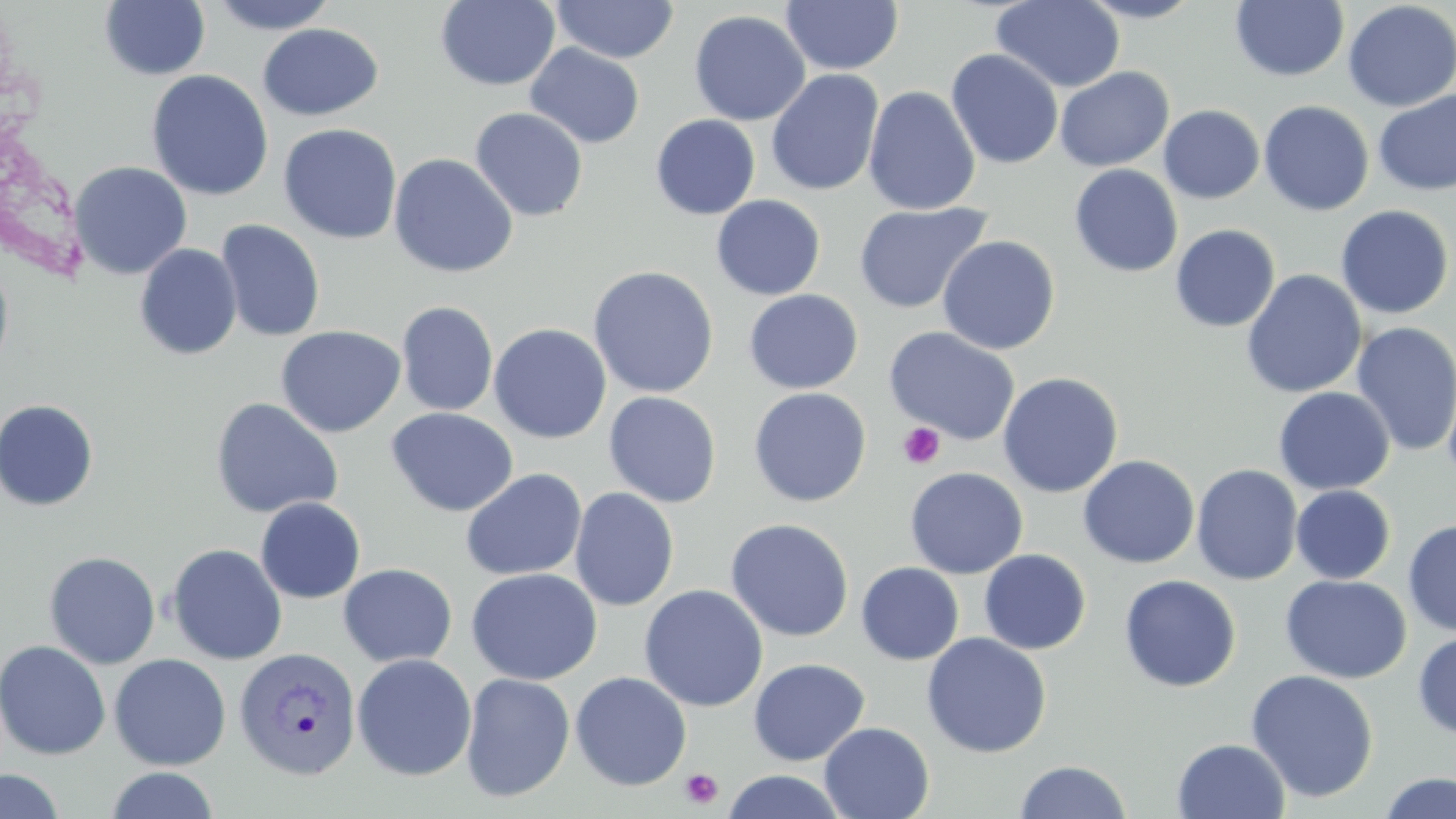 Approximate bounding boxes as [x1, y1, x2, y2] in pixels. Platelet locations: [897, 422, 945, 469], [679, 767, 723, 808]. Uninfected red blood cell locations: [207, 0, 340, 34], [436, 0, 560, 91], [780, 0, 904, 76], [990, 0, 1125, 93], [1077, 0, 1206, 23], [99, 1, 210, 81], [550, 1, 680, 63], [1231, 1, 1349, 82], [1342, 1, 1456, 112], [688, 10, 810, 126], [257, 23, 384, 121], [525, 43, 645, 149], [946, 49, 1064, 169], [1055, 66, 1174, 172], [765, 69, 884, 197], [147, 70, 273, 202], [863, 85, 981, 216], [1373, 89, 1456, 196], [1258, 100, 1374, 216], [1158, 105, 1265, 204], [469, 107, 589, 222], [650, 114, 761, 220], [278, 123, 403, 244], [388, 153, 519, 278], [69, 161, 192, 279], [1069, 164, 1183, 277], [711, 195, 826, 300], [854, 202, 992, 315], [1335, 205, 1455, 320], [216, 219, 326, 342], [1170, 224, 1280, 333], [937, 235, 1060, 355], [134, 243, 242, 361], [0, 260, 14, 379], [587, 265, 720, 398], [1241, 269, 1367, 399], [743, 289, 864, 395], [396, 301, 498, 416], [1351, 321, 1456, 457], [489, 323, 612, 444], [275, 325, 406, 438], [884, 326, 1021, 446], [1439, 354, 1456, 493], [997, 371, 1124, 498], [1273, 386, 1394, 495], [748, 387, 872, 507], [602, 391, 722, 508], [209, 397, 344, 519], [0, 398, 99, 511], [386, 407, 519, 517], [1078, 454, 1200, 569], [1191, 463, 1303, 585], [904, 467, 1028, 579], [460, 468, 587, 581], [1290, 485, 1395, 584], [569, 487, 679, 612], [254, 497, 366, 604], [725, 517, 854, 642], [1403, 518, 1456, 636], [166, 543, 288, 665], [978, 549, 1091, 655], [43, 551, 160, 669], [856, 562, 964, 665], [338, 563, 457, 667], [466, 568, 602, 685], [1119, 574, 1241, 692], [1280, 574, 1412, 684], [639, 584, 768, 712], [1412, 630, 1456, 740], [921, 632, 1051, 758], [0, 640, 111, 760], [108, 653, 231, 771], [352, 653, 476, 781], [747, 658, 870, 766], [1245, 669, 1379, 802], [570, 671, 692, 791], [460, 672, 575, 803], [819, 721, 934, 819], [1172, 738, 1290, 819], [1014, 760, 1133, 819], [104, 767, 221, 818], [0, 769, 66, 818], [721, 770, 848, 818], [1377, 772, 1456, 818]. Plasmodium vivax-infected red blood cell locations: [234, 646, 362, 780]. Slide-level diagnosis: Plasmodium vivax. May-Grünwald-Giemsa stain. Optical microscopy. Thin blood smear. Image is 1456×819 pixels. Single field of view. 1000x magnification.